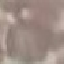
malaria status = uninfected
preparation = thin blood smear
stain = Giemsa
capture = smartphone camera at the microscope eyepiece
image type = cell patch, automatically extracted from a larger field of view and resized to 64 × 64 pixels